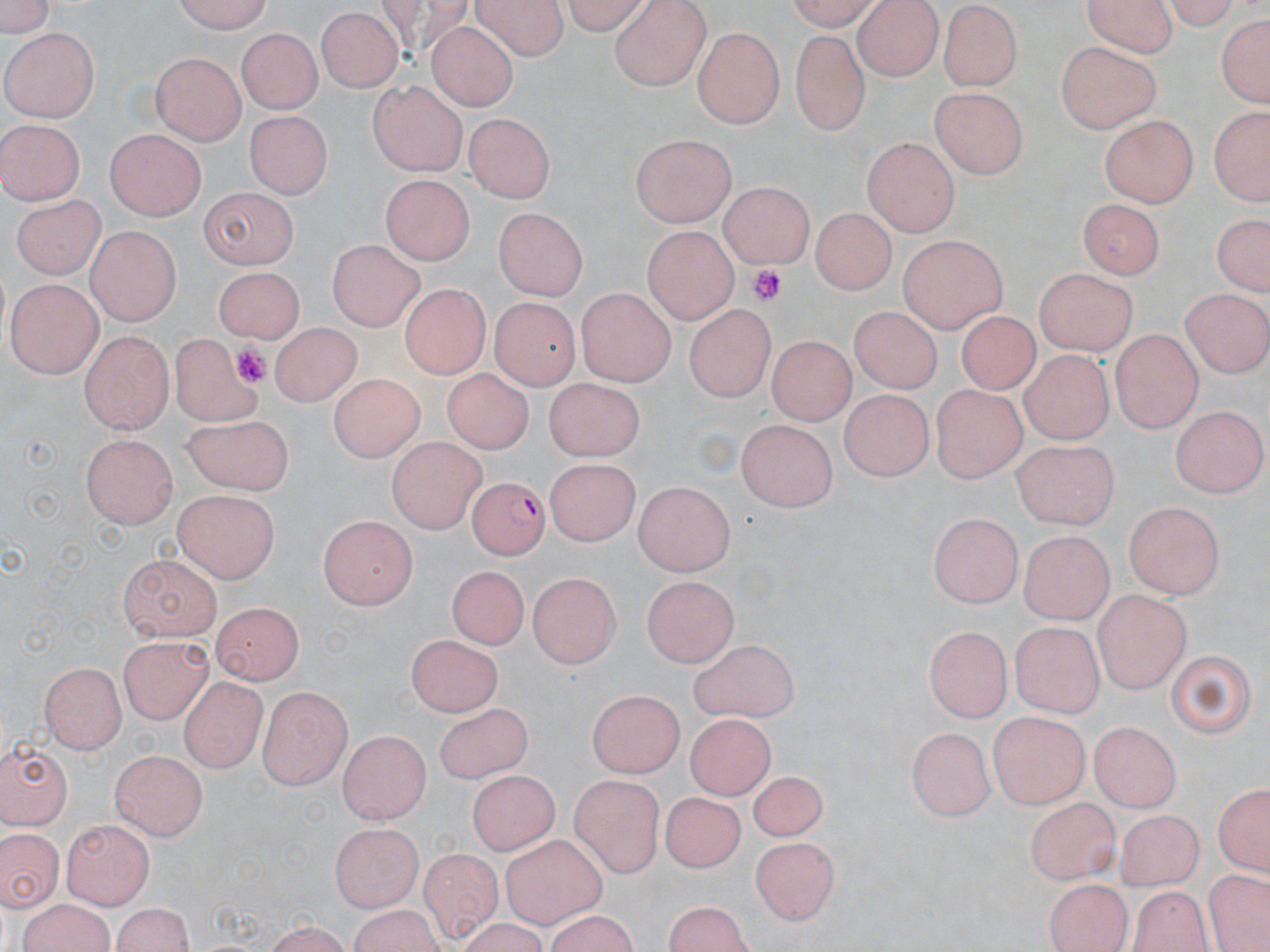
Approximate bounding boxes as named x1/y1/x2/y2 corners in pixels. Uninfected red blood cell locations: (x1=173, y1=0, x2=274, y2=29), (x1=475, y1=0, x2=569, y2=57), (x1=557, y1=0, x2=653, y2=30), (x1=779, y1=0, x2=879, y2=28), (x1=853, y1=0, x2=942, y2=80), (x1=1088, y1=0, x2=1176, y2=53), (x1=0, y1=1, x2=56, y2=38), (x1=608, y1=1, x2=714, y2=90), (x1=1167, y1=3, x2=1244, y2=35), (x1=936, y1=5, x2=1021, y2=90), (x1=315, y1=9, x2=401, y2=93), (x1=1214, y1=10, x2=1269, y2=113), (x1=426, y1=19, x2=517, y2=111), (x1=694, y1=27, x2=783, y2=128), (x1=2, y1=28, x2=101, y2=120), (x1=235, y1=28, x2=320, y2=114), (x1=788, y1=33, x2=868, y2=134), (x1=1055, y1=39, x2=1160, y2=134), (x1=151, y1=54, x2=244, y2=145), (x1=367, y1=79, x2=466, y2=176), (x1=930, y1=88, x2=1027, y2=178), (x1=377, y1=93, x2=470, y2=252), (x1=1207, y1=104, x2=1266, y2=207), (x1=244, y1=110, x2=333, y2=201), (x1=463, y1=111, x2=556, y2=204), (x1=1100, y1=116, x2=1197, y2=207), (x1=1, y1=119, x2=85, y2=206), (x1=104, y1=128, x2=204, y2=220), (x1=631, y1=134, x2=738, y2=227), (x1=863, y1=136, x2=958, y2=236), (x1=379, y1=176, x2=476, y2=266), (x1=718, y1=183, x2=812, y2=269), (x1=196, y1=184, x2=297, y2=267), (x1=13, y1=192, x2=104, y2=281), (x1=1075, y1=198, x2=1167, y2=278), (x1=811, y1=205, x2=895, y2=295), (x1=491, y1=206, x2=590, y2=302), (x1=1210, y1=210, x2=1267, y2=299), (x1=642, y1=223, x2=737, y2=322), (x1=84, y1=226, x2=178, y2=324), (x1=899, y1=233, x2=1009, y2=333), (x1=325, y1=241, x2=425, y2=328), (x1=211, y1=264, x2=304, y2=337), (x1=1034, y1=267, x2=1135, y2=359), (x1=7, y1=275, x2=103, y2=377), (x1=575, y1=288, x2=677, y2=383), (x1=1181, y1=290, x2=1268, y2=377), (x1=488, y1=295, x2=580, y2=389), (x1=686, y1=300, x2=774, y2=394), (x1=848, y1=307, x2=940, y2=392), (x1=953, y1=309, x2=1045, y2=397), (x1=267, y1=323, x2=365, y2=405), (x1=78, y1=328, x2=174, y2=434), (x1=1109, y1=328, x2=1203, y2=431), (x1=166, y1=333, x2=264, y2=437), (x1=768, y1=333, x2=855, y2=422), (x1=1017, y1=350, x2=1114, y2=444), (x1=442, y1=369, x2=532, y2=456), (x1=328, y1=370, x2=424, y2=463), (x1=542, y1=373, x2=639, y2=458), (x1=839, y1=380, x2=930, y2=475), (x1=929, y1=382, x2=1027, y2=482), (x1=1171, y1=404, x2=1265, y2=495), (x1=183, y1=416, x2=293, y2=493), (x1=733, y1=419, x2=839, y2=509), (x1=80, y1=433, x2=177, y2=526), (x1=386, y1=436, x2=485, y2=534), (x1=1008, y1=439, x2=1118, y2=529), (x1=549, y1=455, x2=640, y2=544), (x1=629, y1=484, x2=738, y2=576), (x1=172, y1=491, x2=277, y2=583), (x1=1124, y1=501, x2=1225, y2=596), (x1=928, y1=510, x2=1021, y2=605), (x1=316, y1=517, x2=420, y2=610), (x1=1022, y1=528, x2=1112, y2=626), (x1=117, y1=557, x2=221, y2=643), (x1=440, y1=571, x2=523, y2=651), (x1=526, y1=574, x2=623, y2=667), (x1=641, y1=575, x2=740, y2=663), (x1=1093, y1=590, x2=1192, y2=691), (x1=211, y1=603, x2=300, y2=684), (x1=1010, y1=620, x2=1102, y2=717), (x1=926, y1=624, x2=1010, y2=724), (x1=406, y1=632, x2=501, y2=716), (x1=120, y1=637, x2=212, y2=724), (x1=691, y1=638, x2=799, y2=725), (x1=1164, y1=648, x2=1258, y2=741), (x1=40, y1=659, x2=126, y2=752), (x1=176, y1=677, x2=273, y2=777), (x1=260, y1=684, x2=352, y2=790), (x1=586, y1=687, x2=681, y2=778), (x1=434, y1=703, x2=535, y2=788), (x1=990, y1=710, x2=1090, y2=808), (x1=684, y1=713, x2=774, y2=800), (x1=1087, y1=721, x2=1178, y2=808), (x1=908, y1=726, x2=993, y2=818), (x1=336, y1=731, x2=431, y2=822), (x1=0, y1=737, x2=71, y2=831), (x1=111, y1=750, x2=207, y2=840), (x1=748, y1=767, x2=825, y2=843), (x1=466, y1=769, x2=561, y2=851), (x1=569, y1=774, x2=668, y2=877), (x1=1209, y1=782, x2=1269, y2=875), (x1=658, y1=794, x2=746, y2=877), (x1=1024, y1=795, x2=1119, y2=880), (x1=1114, y1=808, x2=1204, y2=886), (x1=63, y1=819, x2=152, y2=909), (x1=328, y1=821, x2=415, y2=909), (x1=1, y1=825, x2=61, y2=914), (x1=499, y1=835, x2=616, y2=935), (x1=750, y1=836, x2=841, y2=926), (x1=415, y1=846, x2=508, y2=943), (x1=1208, y1=871, x2=1266, y2=950), (x1=1041, y1=877, x2=1134, y2=952), (x1=1124, y1=881, x2=1215, y2=952), (x1=659, y1=898, x2=757, y2=952), (x1=108, y1=902, x2=194, y2=952). Plasmodium falciparum-infected red blood cell locations: (x1=464, y1=478, x2=553, y2=568). Platelet locations: (x1=745, y1=263, x2=788, y2=307), (x1=232, y1=340, x2=275, y2=385). Slide-level diagnosis: Plasmodium falciparum. May-Grünwald-Giemsa stain. Thin blood smear. Captured at 1000x magnification. Light microscopy. One field of a larger specimen. Image is 1270×952 pixels.